Assess this cell for malaria.
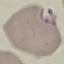
It is parasitized.

Cell patch, automatically extracted from a larger field of view and resized to 64 × 64 pixels. Acquired by smartphone through the microscope eyepiece. Thin smear of blood. Giemsa stain.